Give the extent of all Plasmodium ovale-infected red blood cells.
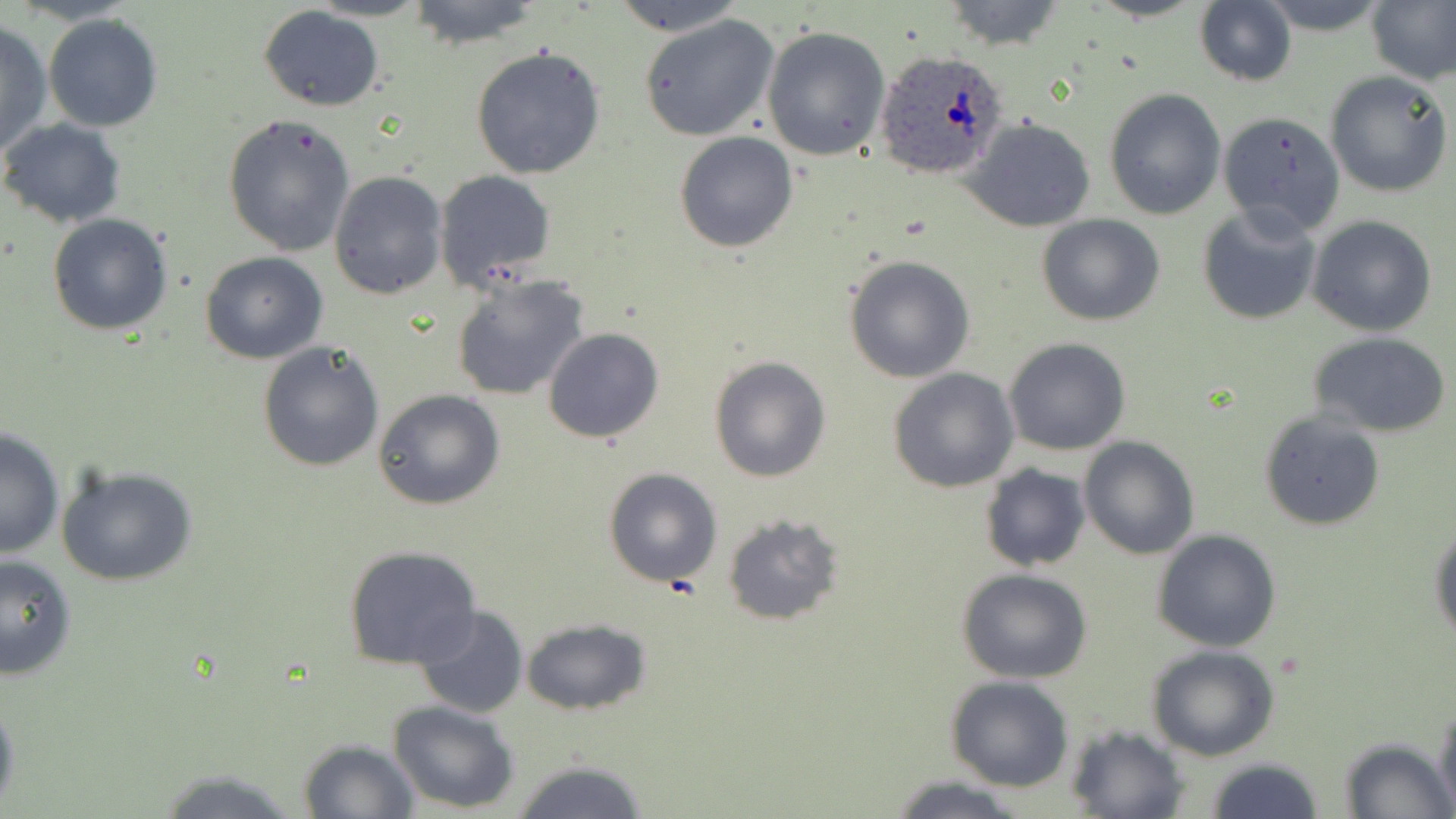
Approximate bounding boxes as (x1, y1, x2, y2) in pixels.
Plasmodium ovale-infected red blood cells: (873, 50, 1010, 176).

slide-level diagnosis = Plasmodium ovale
stain = May-Grünwald-Giemsa
magnification = 1000x
field of view = one of a larger specimen
preparation = thin blood film
modality = optical microscopy
uninfected red blood cell locations = approximate bounding boxes as (x1, y1, x2, y2) in pixels: (308, 0, 432, 21), (403, 0, 545, 48), (614, 0, 744, 37), (938, 0, 1067, 50), (1255, 0, 1395, 33), (1367, 0, 1456, 87), (1194, 1, 1297, 86), (257, 5, 385, 112), (638, 12, 781, 143), (43, 14, 163, 132), (0, 20, 52, 159), (762, 25, 892, 161), (470, 45, 607, 179), (1325, 70, 1453, 198), (1103, 87, 1227, 219), (1226, 88, 1439, 213), (1216, 111, 1346, 235), (223, 114, 358, 256), (964, 116, 1097, 232), (0, 118, 126, 228), (675, 132, 798, 253), (434, 169, 555, 289), (329, 171, 447, 299), (1196, 204, 1322, 325), (48, 213, 173, 335), (1037, 214, 1165, 326), (1307, 216, 1438, 336), (199, 252, 328, 364), (842, 255, 976, 384), (450, 273, 590, 402), (543, 327, 666, 443), (1310, 333, 1452, 438), (1004, 337, 1132, 456), (257, 339, 386, 471), (708, 354, 832, 483), (888, 368, 1018, 494), (373, 388, 506, 511), (1259, 409, 1386, 531), (1, 426, 64, 561), (1079, 436, 1199, 558), (979, 464, 1091, 571), (55, 465, 198, 587), (603, 467, 722, 587), (722, 513, 844, 625), (1429, 526, 1456, 644), (1152, 528, 1282, 652), (343, 545, 482, 670), (0, 553, 76, 681), (955, 568, 1095, 682), (410, 606, 529, 719), (522, 616, 651, 716), (1146, 644, 1282, 762), (943, 675, 1073, 791), (0, 692, 22, 814), (1432, 696, 1456, 818), (389, 700, 521, 815), (1065, 725, 1189, 819), (297, 739, 418, 819), (1338, 739, 1453, 818), (510, 758, 650, 817), (1203, 758, 1324, 818), (150, 765, 309, 818), (889, 776, 1028, 817)
image size = 1456×819 pixels